State which cell type is depicted.
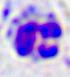
A leukocyte.

Micrograph. 400x magnification.